Describe the morphology of the erythrocytes.
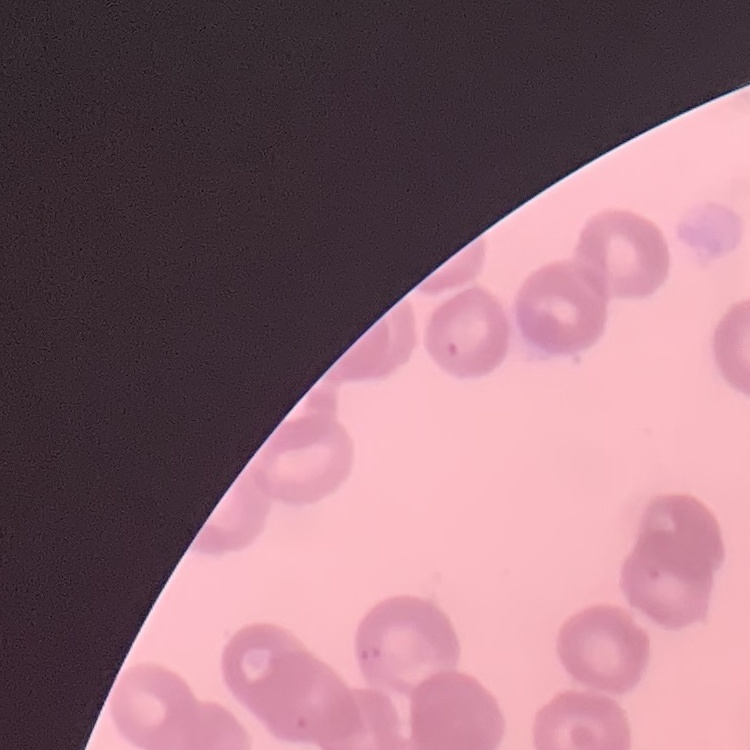
They show rouleaux formation.

One tile cut from a larger photomicrograph. Thin blood smear. Stained with either Field's or Giemsa.